Outline each blood parasite and name the species.
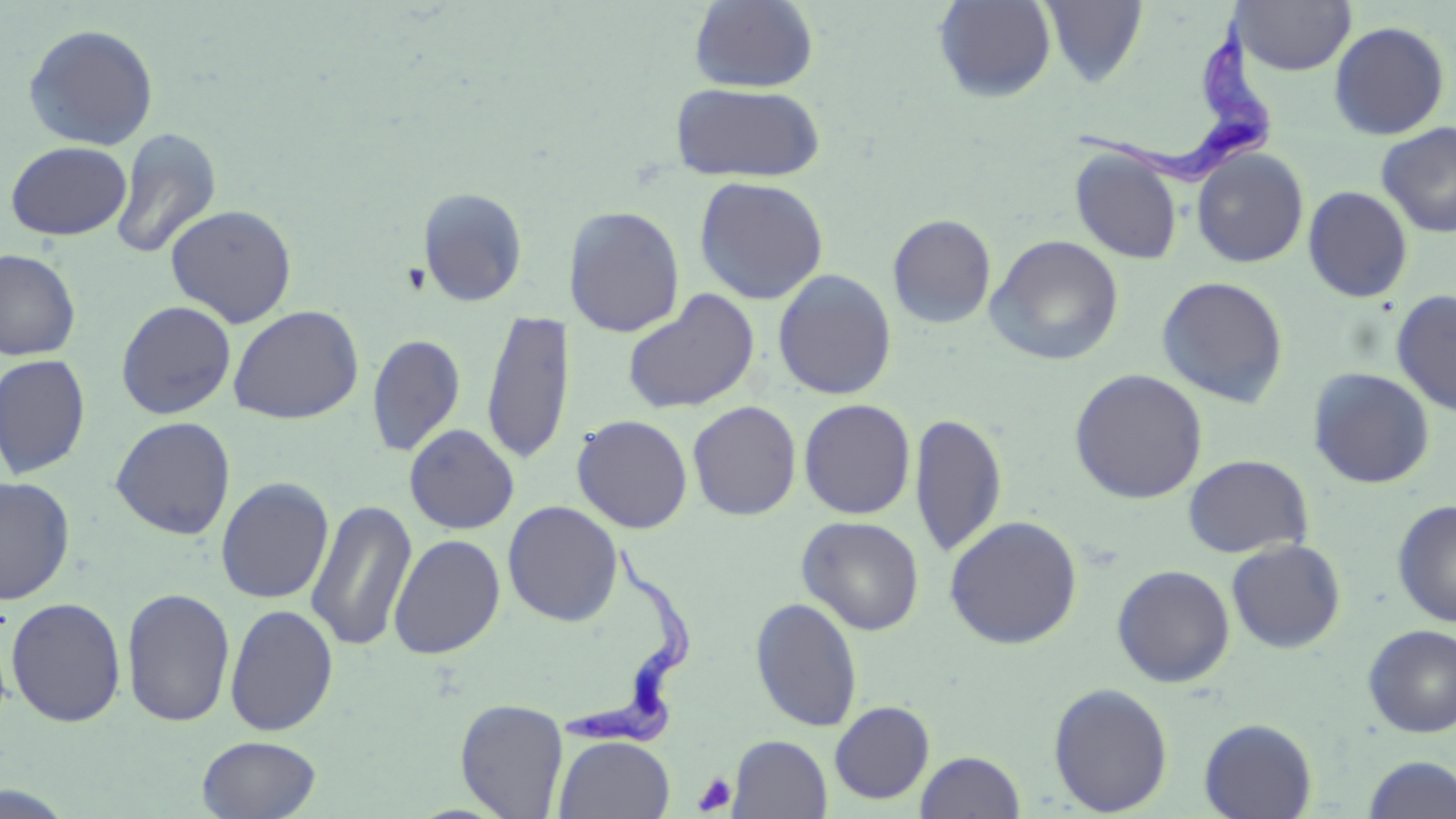
Approximate bounding boxes as named x1/y1/x2/y2 corners in pixels.
Trypanosoma brucei: (x1=1068, y1=10, x2=1274, y2=192), (x1=559, y1=540, x2=696, y2=751).
No Plasmodium falciparum, Plasmodium ovale, Plasmodium malariae, Plasmodium vivax, or Babesia divergens observed.

Summary:
  - Uninfected red blood cell locations: (x1=689, y1=0, x2=819, y2=92), (x1=933, y1=0, x2=1057, y2=103), (x1=1040, y1=1, x2=1148, y2=87), (x1=1233, y1=1, x2=1355, y2=75), (x1=1328, y1=20, x2=1451, y2=140), (x1=22, y1=23, x2=159, y2=151), (x1=669, y1=80, x2=825, y2=183), (x1=1375, y1=122, x2=1456, y2=238), (x1=110, y1=128, x2=222, y2=261), (x1=5, y1=141, x2=133, y2=240), (x1=1070, y1=148, x2=1184, y2=264), (x1=1192, y1=148, x2=1309, y2=268), (x1=693, y1=176, x2=829, y2=305), (x1=418, y1=186, x2=529, y2=307), (x1=1303, y1=186, x2=1413, y2=303), (x1=164, y1=204, x2=298, y2=328), (x1=564, y1=205, x2=685, y2=337), (x1=887, y1=214, x2=996, y2=329), (x1=986, y1=235, x2=1124, y2=366), (x1=0, y1=248, x2=81, y2=360), (x1=772, y1=269, x2=897, y2=400), (x1=1156, y1=275, x2=1289, y2=408), (x1=622, y1=288, x2=761, y2=415), (x1=1391, y1=289, x2=1456, y2=416), (x1=116, y1=300, x2=237, y2=420), (x1=228, y1=305, x2=364, y2=424), (x1=481, y1=309, x2=574, y2=466), (x1=366, y1=333, x2=466, y2=456), (x1=0, y1=354, x2=91, y2=479), (x1=1308, y1=367, x2=1435, y2=488), (x1=1069, y1=368, x2=1208, y2=504), (x1=798, y1=398, x2=916, y2=519), (x1=687, y1=400, x2=802, y2=521), (x1=909, y1=412, x2=1008, y2=559), (x1=571, y1=414, x2=693, y2=534), (x1=110, y1=416, x2=236, y2=540), (x1=404, y1=423, x2=519, y2=534), (x1=1183, y1=454, x2=1313, y2=558), (x1=0, y1=476, x2=76, y2=604), (x1=215, y1=477, x2=335, y2=604), (x1=306, y1=499, x2=418, y2=652), (x1=1392, y1=499, x2=1456, y2=627), (x1=502, y1=501, x2=624, y2=626), (x1=944, y1=515, x2=1083, y2=649), (x1=797, y1=516, x2=924, y2=635), (x1=388, y1=534, x2=505, y2=659), (x1=1226, y1=539, x2=1346, y2=653), (x1=1111, y1=564, x2=1235, y2=688), (x1=122, y1=587, x2=235, y2=728), (x1=750, y1=596, x2=863, y2=732), (x1=5, y1=597, x2=127, y2=727), (x1=224, y1=603, x2=339, y2=736), (x1=1362, y1=625, x2=1456, y2=737), (x1=1048, y1=682, x2=1173, y2=816), (x1=455, y1=698, x2=569, y2=819), (x1=829, y1=700, x2=934, y2=804), (x1=1198, y1=718, x2=1318, y2=819), (x1=197, y1=735, x2=321, y2=819), (x1=553, y1=735, x2=675, y2=818), (x1=727, y1=735, x2=832, y2=818), (x1=915, y1=750, x2=1026, y2=818), (x1=1361, y1=754, x2=1455, y2=818)
  - Platelet locations: (x1=401, y1=263, x2=431, y2=294), (x1=692, y1=772, x2=737, y2=815)
  - Slide-level diagnosis: Trypanosoma brucei
  - Magnification: 1000x
  - Image size: 1456×819 pixels
  - Field of view: one of a larger specimen
  - Modality: light microscopy
  - Preparation: thin blood smear
  - Stain: May-Grünwald-Giemsa